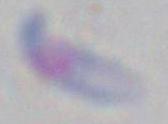 Photomicrograph. Toxoplasma gondii is shown. Captured at 1000x magnification.